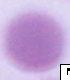
A red blood cell is seen. Captured at 1000x magnification. Photomicrograph.